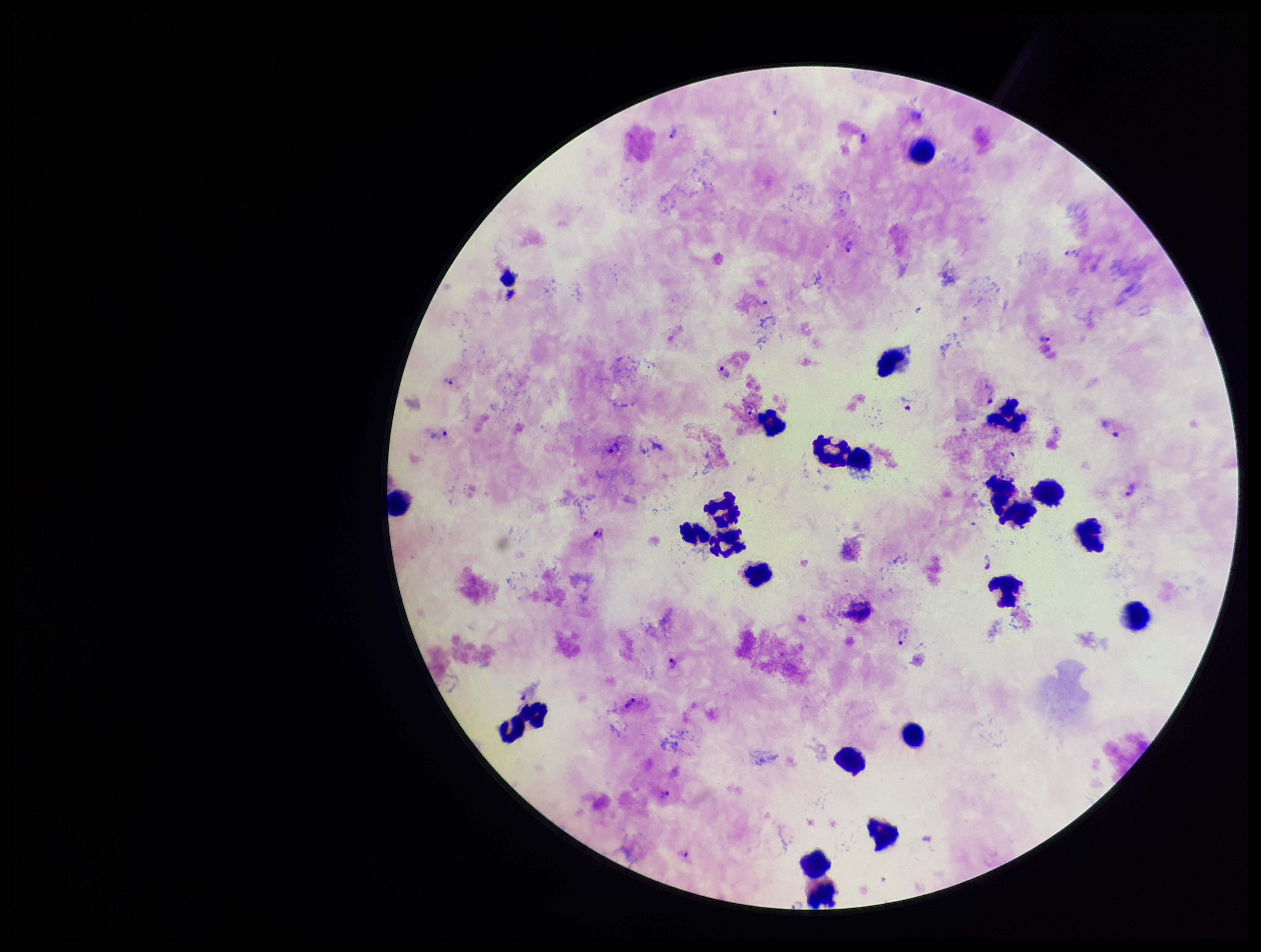
patient malaria status = infected
stain = Giemsa
field of view = one from this slide
image size = 1261×952 pixels
species reported for this patient = Plasmodium vivax
leukocyte count = 23
preparation = thick blood smear
Plasmodium parasites = detected
capture = smartphone photograph through the microscope eyepiece
parasite count = 26